Outline every Plasmodium parasite.
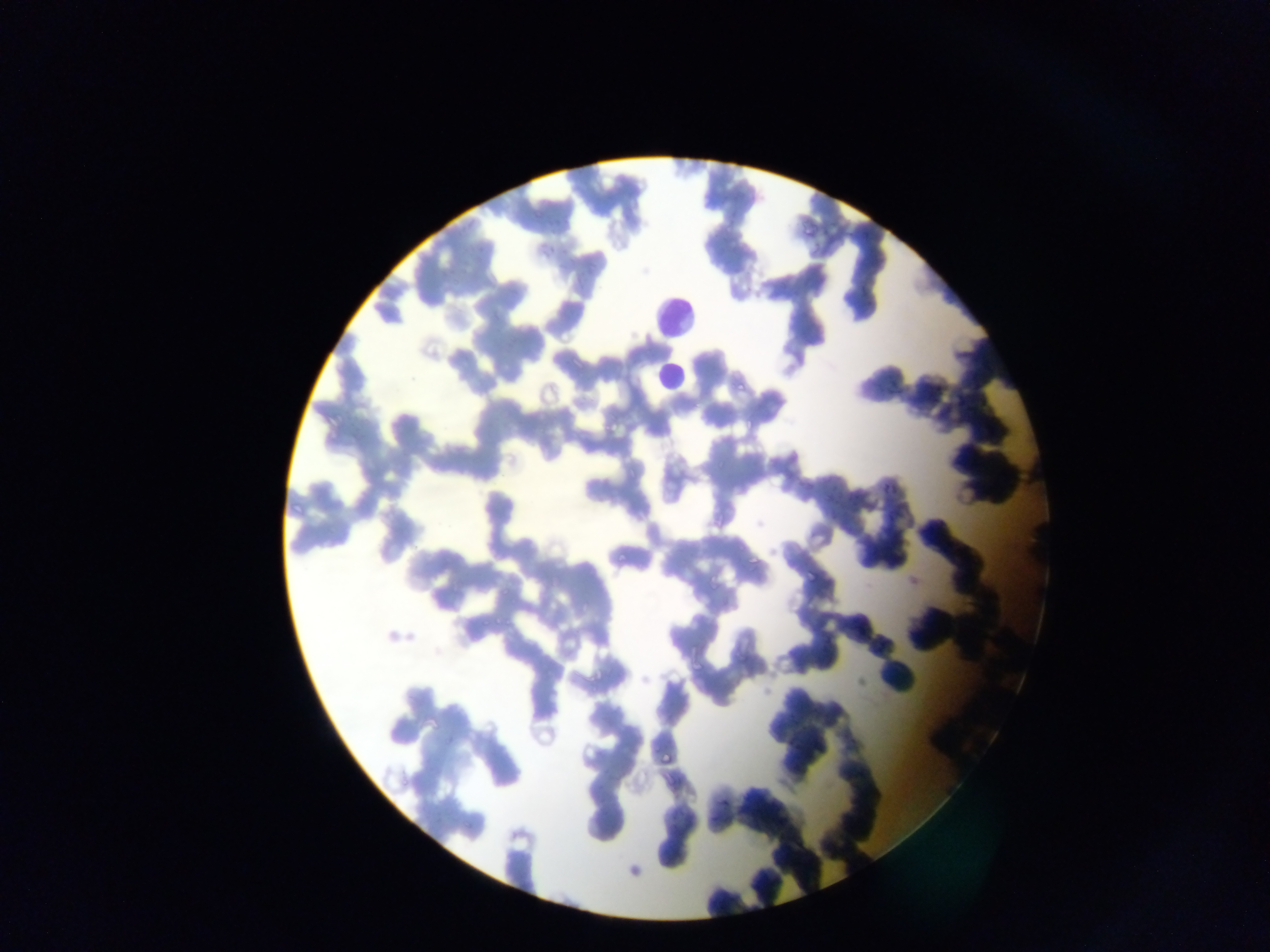

Approximate bounding boxes as [left, top, right, bottom] in pixels.
Plasmodium parasites: [736, 382, 746, 395], [747, 415, 756, 430], [604, 423, 611, 431], [752, 444, 764, 453], [718, 460, 726, 468], [799, 483, 813, 489], [882, 483, 890, 494], [890, 485, 900, 493], [290, 501, 305, 517], [616, 550, 625, 563], [747, 554, 758, 566], [707, 581, 718, 596], [502, 584, 513, 598], [582, 601, 592, 614], [495, 617, 504, 628], [482, 618, 490, 628], [505, 619, 514, 628], [692, 662, 705, 673], [659, 752, 675, 765], [399, 780, 410, 788], [462, 817, 476, 833].

preparation: thin blood smear
leukocyte_locations: 'approximate bounding boxes as [left, top, right, bottom] in pixels: [640, 278, 696, 347], [646, 361, 692, 401]'
country: Ghana
image_size: 1270×952 pixels
capture: mobile-phone photograph through a microscope
field_of_view: single